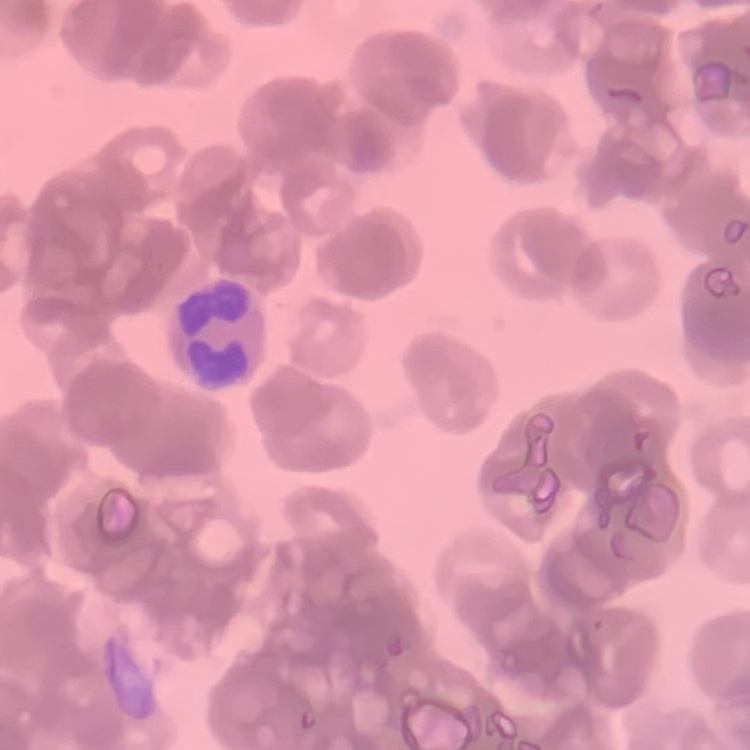
red blood cell morphology = rouleaux formation
preparation = thin blood film
stain = Field's or Giemsa
image type = square crop of a larger photomicrograph